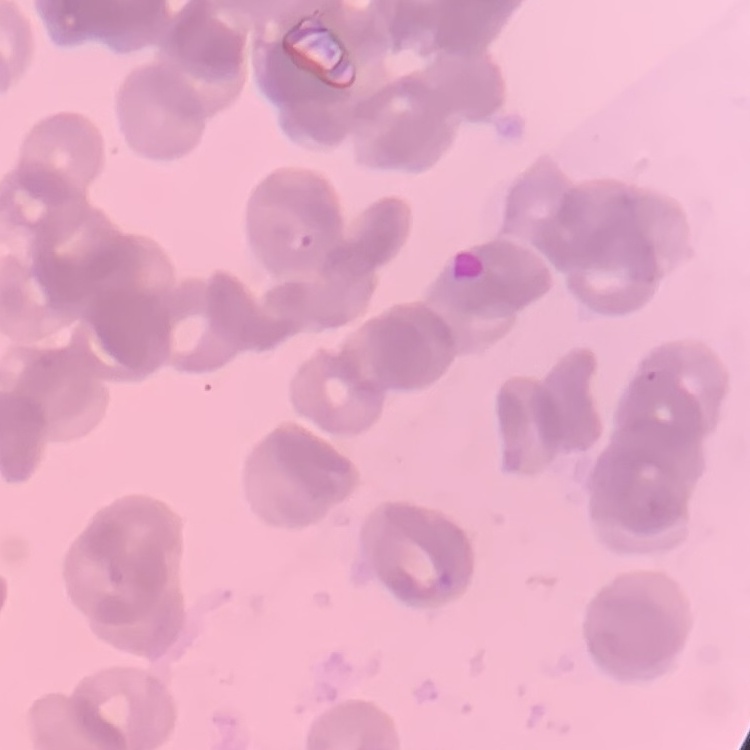 The red blood cells show rouleaux formation. Thin blood smear. Stained with either Field's or Giemsa. Square crop of a larger photomicrograph.